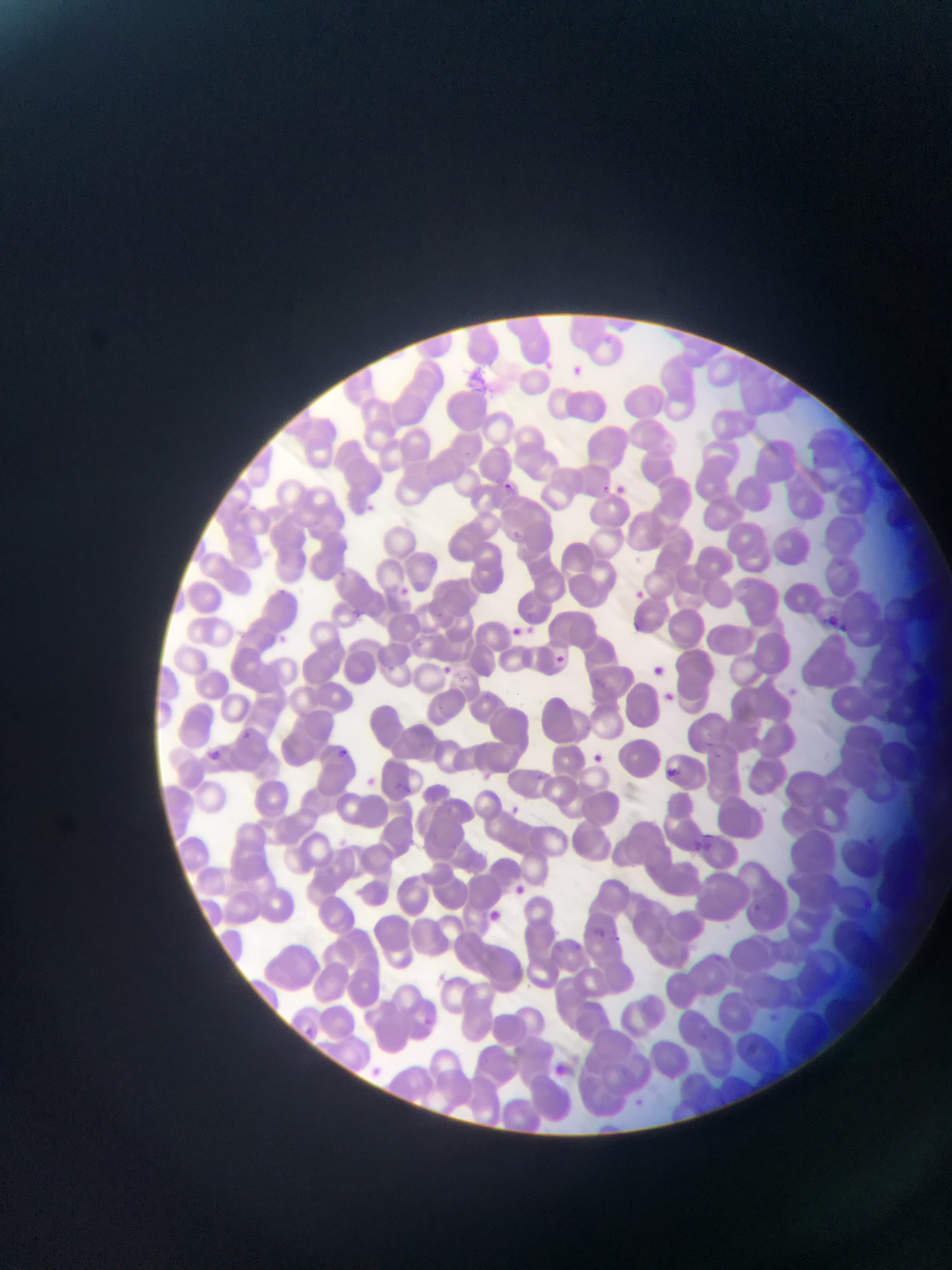 Approximate bounding boxes as (left, top, right, bottom) in pixels. Plasmodium parasite locations: (602, 331, 611, 343), (543, 357, 556, 368), (572, 364, 584, 377), (504, 479, 514, 490), (602, 483, 612, 492), (366, 499, 380, 515), (337, 568, 350, 578), (402, 583, 421, 605), (277, 586, 291, 595), (631, 588, 646, 606), (822, 609, 840, 626), (510, 622, 524, 636), (837, 622, 853, 632), (557, 654, 571, 664), (443, 666, 452, 674), (240, 730, 259, 740), (338, 745, 351, 754), (708, 749, 721, 760), (591, 751, 605, 764), (661, 766, 681, 779), (702, 827, 716, 844), (864, 837, 878, 848), (693, 839, 703, 849), (753, 902, 765, 913), (596, 927, 609, 938), (611, 936, 625, 942), (770, 1009, 777, 1017), (306, 1025, 314, 1037), (748, 1039, 764, 1057), (366, 1064, 386, 1075) | approximate (x, y) pixel centers of objects too small to bound: (530, 629). Photographed through a microscope with a mobile-phone camera. Image is 952×1270 pixels. Thin blood smear. Single field of view. Collected in Ghana.